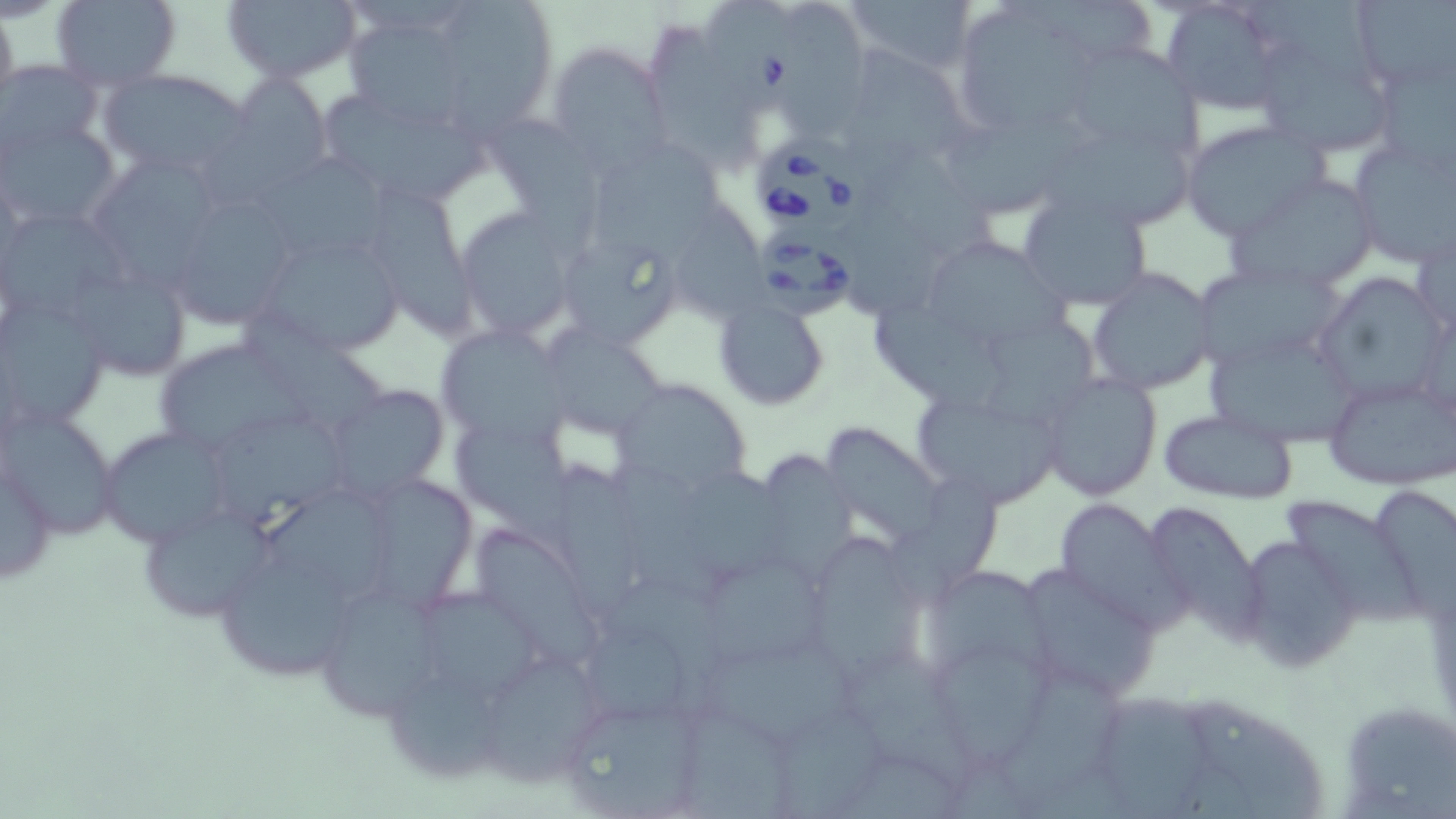

slide-level diagnosis = Babesia divergens
image size = 1456×819 pixels
field of view = one of a larger specimen
preparation = thin blood film
magnification = 1000x
uninfected red blood cell locations = approximate bounding boxes as (x1, y1, x2, y2) in pixels: (220, 0, 364, 83), (444, 0, 559, 132), (790, 0, 869, 138), (846, 0, 980, 76), (1001, 0, 1156, 56), (1158, 0, 1294, 114), (1252, 0, 1380, 79), (50, 1, 181, 88), (1350, 1, 1456, 92), (0, 3, 19, 117), (959, 14, 1092, 126), (352, 21, 462, 134), (1249, 30, 1398, 157), (545, 41, 669, 170), (847, 41, 974, 161), (653, 44, 757, 176), (1078, 48, 1205, 155), (1368, 52, 1456, 183), (2, 59, 103, 160), (99, 67, 255, 179), (208, 74, 333, 204), (318, 87, 492, 210), (487, 108, 604, 254), (951, 109, 1082, 214), (0, 117, 123, 233), (1180, 120, 1326, 239), (1347, 136, 1455, 268), (862, 137, 993, 254), (1048, 138, 1196, 223), (598, 147, 721, 262), (258, 159, 392, 257), (99, 167, 215, 286), (1225, 172, 1383, 291), (367, 186, 478, 337), (1016, 189, 1154, 310), (847, 191, 941, 315), (674, 194, 764, 325), (181, 200, 291, 324), (1, 206, 131, 326), (455, 206, 581, 341), (557, 233, 681, 349), (258, 238, 409, 346), (925, 243, 1077, 336), (1201, 262, 1346, 366), (1087, 267, 1216, 395), (75, 271, 187, 374), (1313, 272, 1447, 410), (713, 297, 830, 408), (1, 298, 110, 429), (244, 305, 383, 426), (878, 306, 1001, 414), (985, 312, 1098, 420), (434, 326, 566, 446), (546, 327, 669, 443), (162, 340, 308, 447), (1213, 340, 1355, 439), (1038, 371, 1162, 500), (1326, 375, 1456, 489), (613, 380, 751, 494), (334, 384, 449, 493), (921, 399, 1056, 501), (1, 405, 120, 540), (1157, 407, 1299, 504), (214, 416, 353, 534), (98, 426, 233, 549), (830, 426, 942, 543), (458, 429, 573, 542), (765, 448, 856, 577), (1, 451, 57, 588), (559, 461, 635, 615), (602, 464, 729, 606), (375, 473, 471, 612), (887, 474, 1001, 609), (684, 476, 792, 581), (1379, 489, 1456, 619), (267, 493, 405, 599), (1049, 498, 1185, 628), (1290, 502, 1421, 624), (1142, 504, 1263, 638), (146, 511, 272, 620), (473, 529, 599, 656), (1237, 534, 1360, 672), (817, 538, 925, 688), (217, 551, 357, 675), (706, 564, 823, 663), (935, 568, 1058, 678), (1032, 568, 1160, 697), (614, 580, 729, 715), (423, 587, 537, 699), (334, 591, 439, 717), (586, 630, 695, 722), (693, 637, 856, 740), (933, 645, 1052, 764), (847, 650, 968, 788), (481, 657, 601, 788), (1006, 671, 1123, 798), (396, 673, 498, 779), (1106, 686, 1209, 819), (555, 691, 712, 817), (1193, 699, 1322, 819), (1352, 705, 1456, 818), (683, 706, 786, 817), (779, 709, 882, 818), (845, 749, 974, 819)
stain = May-Grünwald-Giemsa
Babesia divergens-infected red blood cell locations = approximate bounding boxes as (x1, y1, x2, y2) in pixels: (708, 1, 807, 119), (752, 137, 868, 240), (756, 225, 864, 321)
modality = optical microscopy